Classify this cell by malaria status.
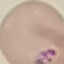
Uninfected.

stain: Giemsa
preparation: thin blood film
capture: smartphone through the microscope eyepiece
image_type: automatically extracted cell patch, resized to 64 × 64 pixels